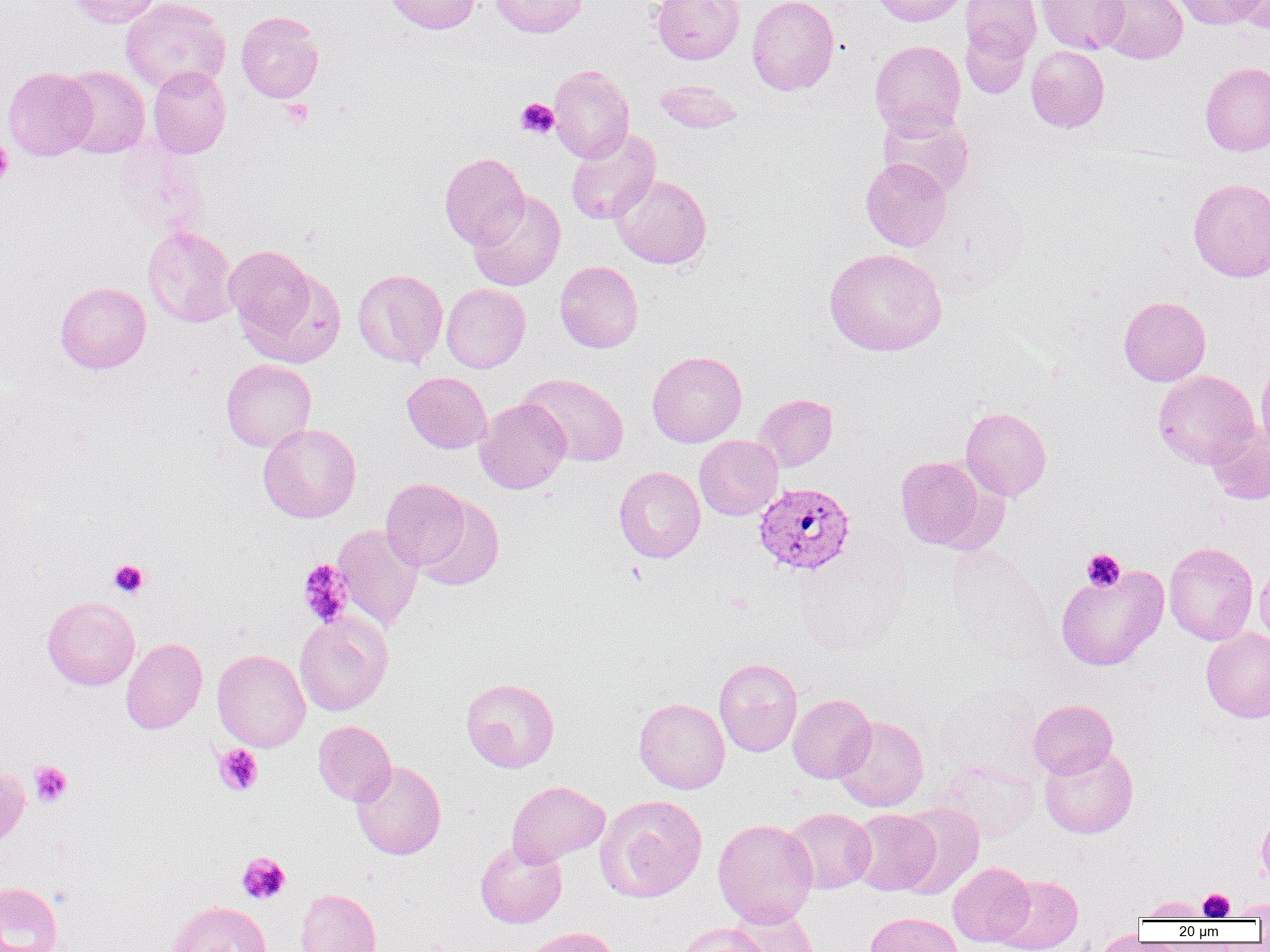
Plasmodium vivax-infected red blood cell locations = approximate bounding boxes as named x1/y1/x2/y2 corners in pixels: (x1=754, y1=482, x2=855, y2=578)
slide-level diagnosis = Plasmodium vivax
platelet locations = approximate bounding boxes as named x1/y1/x2/y2 corners in pixels: (x1=515, y1=98, x2=559, y2=138), (x1=279, y1=99, x2=313, y2=130), (x1=0, y1=138, x2=13, y2=185), (x1=1081, y1=549, x2=1125, y2=592), (x1=109, y1=559, x2=149, y2=599), (x1=298, y1=560, x2=354, y2=628), (x1=214, y1=744, x2=263, y2=795), (x1=29, y1=761, x2=72, y2=807), (x1=237, y1=852, x2=290, y2=904), (x1=1199, y1=889, x2=1235, y2=920)
magnification = 1000x
uninfected red blood cell locations = approximate bounding boxes as named x1/y1/x2/y2 corners in pixels: (x1=67, y1=0, x2=162, y2=28), (x1=120, y1=0, x2=231, y2=95), (x1=384, y1=0, x2=481, y2=34), (x1=490, y1=0, x2=588, y2=37), (x1=652, y1=0, x2=744, y2=63), (x1=747, y1=0, x2=840, y2=95), (x1=868, y1=0, x2=969, y2=26), (x1=1036, y1=0, x2=1129, y2=55), (x1=1097, y1=0, x2=1188, y2=64), (x1=1171, y1=0, x2=1264, y2=29), (x1=960, y1=1, x2=1041, y2=65), (x1=1232, y1=1, x2=1270, y2=33), (x1=236, y1=11, x2=324, y2=103), (x1=960, y1=21, x2=1033, y2=100), (x1=870, y1=40, x2=966, y2=138), (x1=1026, y1=45, x2=1110, y2=133), (x1=1200, y1=62, x2=1270, y2=156), (x1=549, y1=64, x2=634, y2=163), (x1=148, y1=65, x2=231, y2=158), (x1=60, y1=66, x2=150, y2=158), (x1=3, y1=67, x2=97, y2=160), (x1=654, y1=79, x2=743, y2=134), (x1=878, y1=109, x2=975, y2=198), (x1=565, y1=129, x2=660, y2=225), (x1=115, y1=139, x2=210, y2=243), (x1=439, y1=152, x2=529, y2=249), (x1=861, y1=157, x2=952, y2=251), (x1=611, y1=174, x2=712, y2=269), (x1=1188, y1=178, x2=1270, y2=282), (x1=467, y1=190, x2=565, y2=291), (x1=142, y1=225, x2=238, y2=327), (x1=224, y1=245, x2=321, y2=349), (x1=824, y1=248, x2=947, y2=356), (x1=555, y1=260, x2=643, y2=353), (x1=353, y1=268, x2=448, y2=369), (x1=55, y1=282, x2=151, y2=373), (x1=441, y1=283, x2=530, y2=373), (x1=1118, y1=296, x2=1211, y2=386), (x1=647, y1=350, x2=747, y2=447), (x1=1256, y1=358, x2=1270, y2=456), (x1=221, y1=359, x2=316, y2=452), (x1=1153, y1=369, x2=1259, y2=468), (x1=402, y1=372, x2=492, y2=453), (x1=518, y1=373, x2=629, y2=467), (x1=754, y1=393, x2=837, y2=472), (x1=475, y1=397, x2=571, y2=494), (x1=960, y1=407, x2=1052, y2=501), (x1=258, y1=423, x2=361, y2=523), (x1=1206, y1=425, x2=1270, y2=505), (x1=694, y1=435, x2=783, y2=520), (x1=895, y1=455, x2=991, y2=551), (x1=614, y1=466, x2=705, y2=563), (x1=381, y1=478, x2=471, y2=571), (x1=414, y1=495, x2=504, y2=591), (x1=332, y1=524, x2=424, y2=631), (x1=793, y1=537, x2=911, y2=655), (x1=1163, y1=542, x2=1258, y2=645), (x1=1255, y1=558, x2=1270, y2=647), (x1=1055, y1=564, x2=1169, y2=671), (x1=42, y1=597, x2=140, y2=690), (x1=294, y1=611, x2=392, y2=716), (x1=1201, y1=628, x2=1270, y2=723), (x1=121, y1=638, x2=207, y2=734), (x1=212, y1=649, x2=311, y2=751), (x1=714, y1=658, x2=802, y2=756), (x1=461, y1=678, x2=559, y2=772), (x1=936, y1=680, x2=1047, y2=782), (x1=788, y1=693, x2=876, y2=783), (x1=634, y1=697, x2=730, y2=794), (x1=1029, y1=699, x2=1118, y2=779), (x1=833, y1=716, x2=929, y2=812), (x1=313, y1=720, x2=396, y2=805), (x1=1039, y1=744, x2=1138, y2=838), (x1=351, y1=760, x2=446, y2=860), (x1=933, y1=760, x2=1041, y2=842), (x1=0, y1=765, x2=30, y2=854), (x1=507, y1=781, x2=609, y2=866), (x1=595, y1=794, x2=707, y2=902), (x1=894, y1=803, x2=984, y2=900), (x1=783, y1=807, x2=876, y2=893), (x1=849, y1=808, x2=939, y2=896), (x1=1256, y1=810, x2=1270, y2=889), (x1=712, y1=818, x2=818, y2=927), (x1=475, y1=839, x2=567, y2=928), (x1=948, y1=862, x2=1035, y2=946), (x1=995, y1=875, x2=1083, y2=952), (x1=0, y1=881, x2=64, y2=952), (x1=296, y1=888, x2=381, y2=952), (x1=1138, y1=896, x2=1211, y2=921), (x1=1229, y1=899, x2=1269, y2=920), (x1=167, y1=901, x2=271, y2=952), (x1=728, y1=905, x2=820, y2=952), (x1=864, y1=912, x2=963, y2=952), (x1=675, y1=923, x2=772, y2=952), (x1=521, y1=927, x2=621, y2=952), (x1=1089, y1=930, x2=1151, y2=952)
field of view = single
image size = 1270×952 pixels
modality = optical microscopy
preparation = thin blood smear